Outline each blood parasite and name the species.
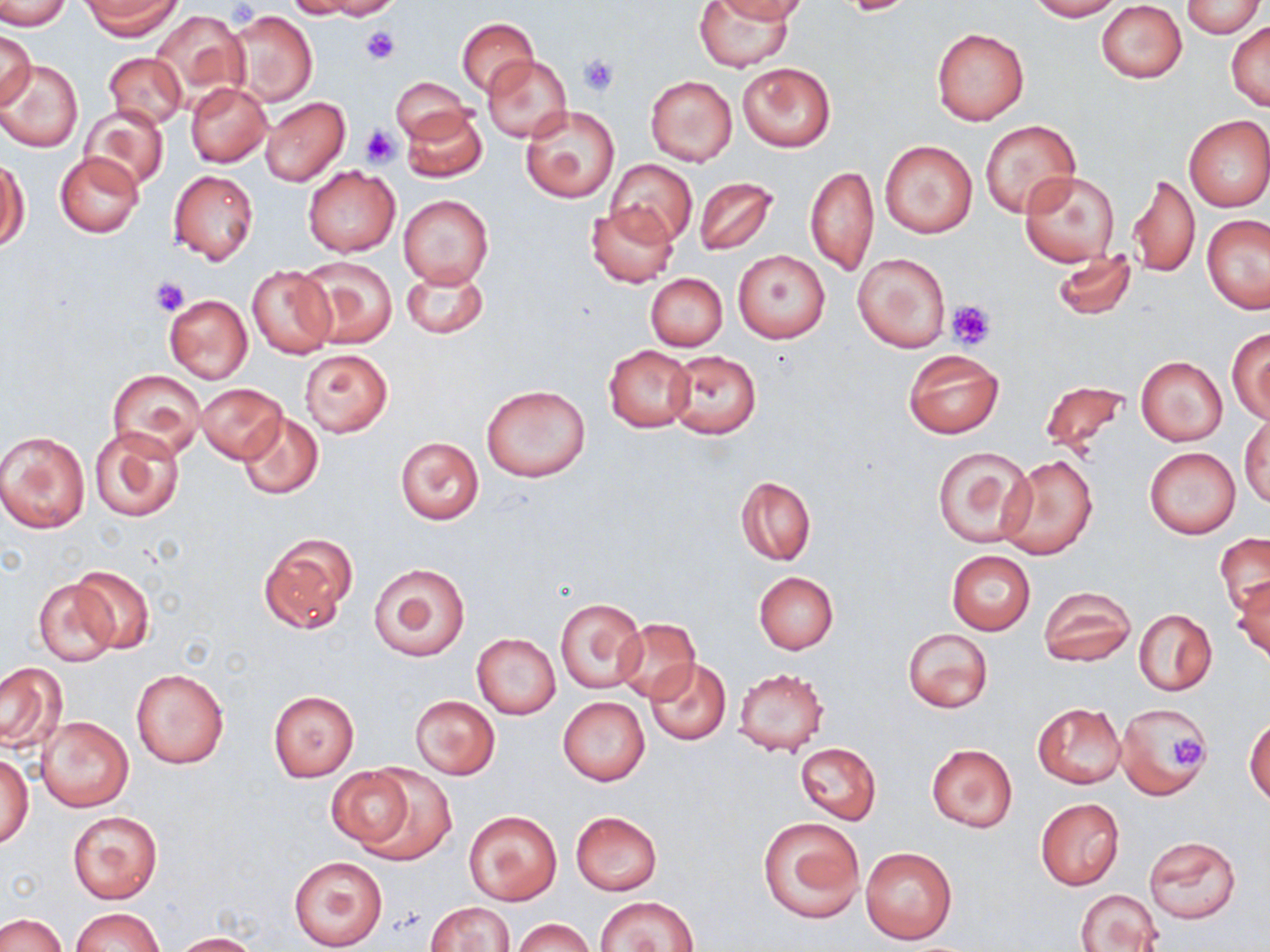
No blood parasites observed.

Summary:
  - Coordinate format: approximate bounding boxes as (x1, y1, x2, y2) in pixels
  - Uninfected red blood cell locations: (0, 0, 71, 30), (84, 0, 179, 38), (284, 0, 370, 18), (318, 0, 398, 19), (695, 0, 796, 72), (712, 0, 805, 22), (1026, 0, 1122, 20), (1182, 0, 1264, 38), (1097, 2, 1187, 83), (226, 10, 317, 107), (151, 11, 246, 104), (455, 18, 538, 96), (1226, 20, 1270, 111), (931, 27, 1030, 125), (2, 28, 36, 111), (103, 53, 187, 129), (482, 55, 572, 142), (0, 59, 83, 152), (736, 62, 836, 151), (645, 75, 738, 167), (391, 78, 471, 144), (186, 82, 271, 167), (260, 97, 350, 186), (520, 105, 619, 203), (80, 106, 169, 191), (402, 107, 487, 183), (1183, 114, 1270, 212), (981, 119, 1079, 218), (879, 140, 979, 237), (54, 152, 143, 238), (1, 157, 29, 251), (606, 159, 696, 246), (805, 166, 877, 276), (303, 167, 399, 257), (167, 169, 259, 266), (1020, 170, 1119, 267), (1128, 175, 1200, 278), (693, 177, 778, 256), (399, 194, 493, 289), (585, 204, 677, 287), (1202, 214, 1270, 313), (734, 250, 829, 344), (1051, 250, 1138, 319), (853, 252, 950, 353), (297, 255, 398, 349), (402, 264, 488, 339), (247, 265, 335, 358), (644, 273, 727, 351), (164, 294, 253, 384), (1227, 328, 1270, 424), (604, 344, 696, 432), (903, 349, 1004, 438), (300, 350, 392, 436), (667, 350, 761, 438), (1135, 355, 1228, 446), (107, 370, 205, 460), (1040, 379, 1132, 462), (196, 383, 286, 463), (481, 383, 591, 482), (238, 412, 324, 499), (1240, 416, 1269, 509), (90, 427, 185, 522), (0, 430, 90, 533), (395, 437, 484, 524), (932, 444, 1037, 548), (1145, 447, 1240, 538), (998, 456, 1097, 559), (736, 476, 816, 565), (257, 532, 357, 634), (1215, 533, 1270, 616), (945, 550, 1037, 635), (368, 560, 471, 661), (69, 565, 156, 654), (753, 571, 838, 654), (1231, 577, 1269, 668), (34, 578, 122, 668), (1038, 586, 1136, 668), (555, 597, 646, 693), (1134, 610, 1216, 695), (611, 619, 701, 705), (902, 627, 993, 714), (471, 633, 561, 719), (644, 658, 730, 744), (0, 661, 67, 753), (131, 667, 230, 769), (734, 668, 829, 756), (268, 690, 359, 780), (410, 695, 500, 778), (558, 696, 650, 785), (1033, 702, 1126, 788), (1115, 704, 1212, 798), (38, 716, 134, 813), (1245, 716, 1270, 808), (794, 742, 881, 825), (925, 744, 1018, 833), (1, 750, 33, 850), (326, 766, 418, 852), (355, 766, 457, 866), (1035, 798, 1124, 890), (463, 810, 563, 906), (67, 811, 163, 903), (570, 811, 662, 895), (759, 818, 863, 923), (1143, 836, 1243, 926), (860, 846, 958, 945), (289, 856, 388, 950), (1075, 889, 1164, 952), (596, 896, 698, 951), (426, 901, 515, 951), (72, 908, 164, 952), (0, 913, 66, 952), (513, 918, 593, 952), (173, 932, 260, 951)
  - Platelet locations: (843, 0, 911, 17), (359, 26, 400, 65), (576, 54, 620, 96), (360, 124, 401, 167), (151, 277, 190, 316), (946, 300, 994, 349), (1162, 731, 1209, 772)
  - Slide-level diagnosis: no evidence of blood parasites
  - Magnification: 1000x
  - Modality: optical microscopy
  - Image size: 1270×952 pixels
  - Preparation: thin blood smear
  - Stain: May-Grünwald-Giemsa
  - Field of view: single